State which cell type is depicted.
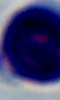
This is a leukocyte.

modality = micrograph
magnification = 1000x